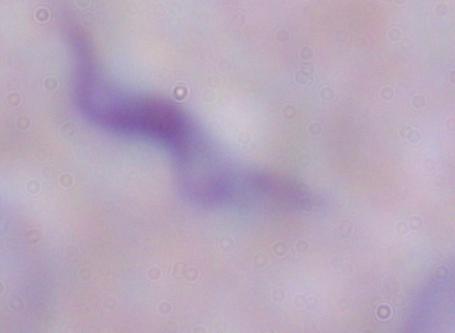

modality = photomicrograph
identification = trypanosome
magnification = 1000x